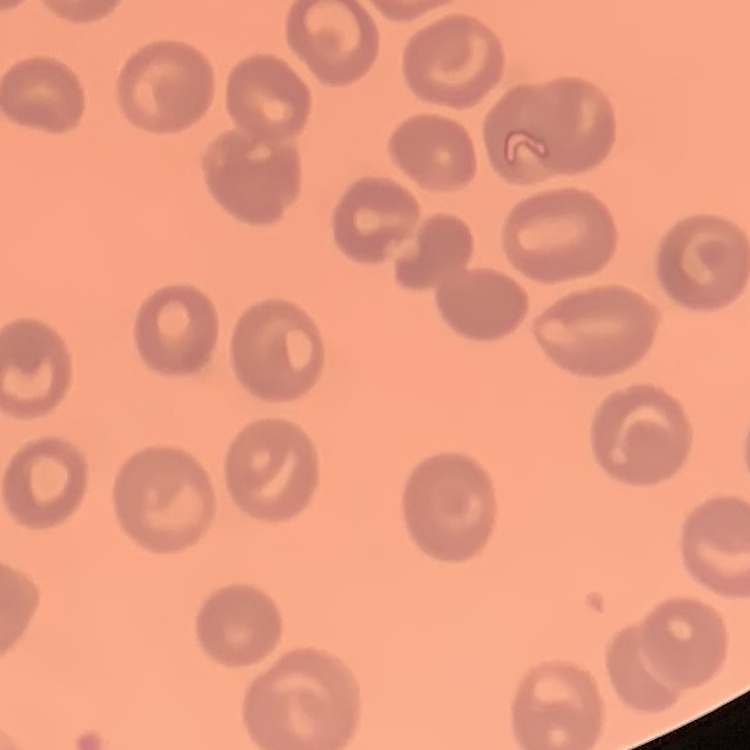
The erythrocytes exhibit no rouleaux formation. Field's or Giemsa stain. Square crop of a larger photomicrograph. Thin blood film.